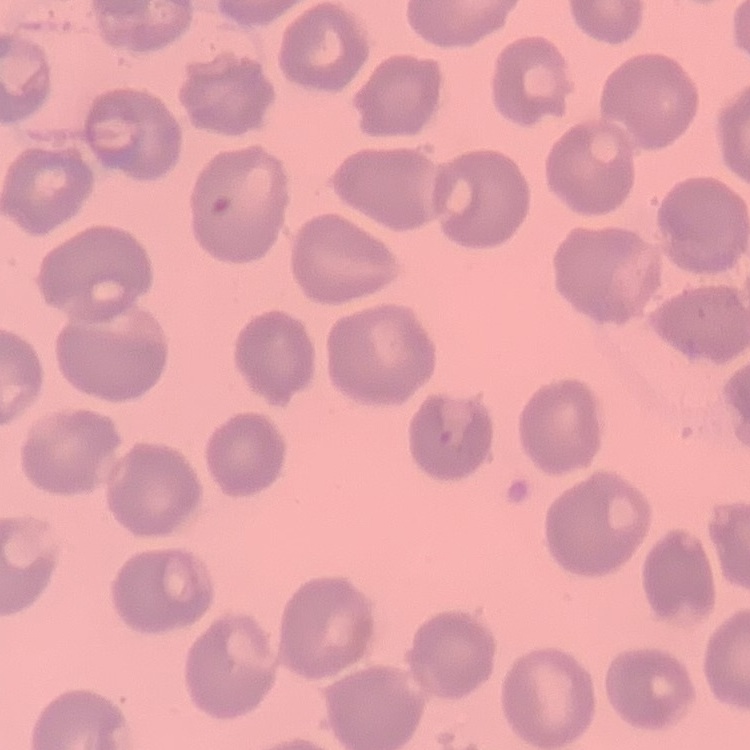
The red blood cells exhibit no rouleaux formation. Thin peripheral smear. One tile cut from a larger photomicrograph. Field's or Giemsa stain.